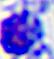
identification: white blood cell
modality: photomicrograph
magnification: 400x